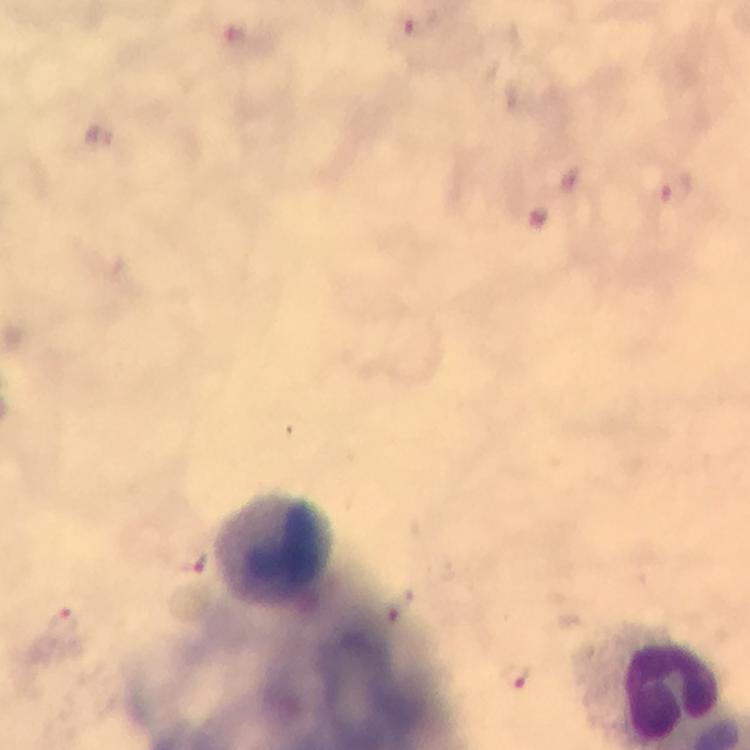

Approximate centers as (x, y) in pixels.
Summary:
  - Malaria parasite locations: (413, 25), (97, 136), (678, 189), (191, 562), (404, 605), (63, 628), (517, 677)
  - Leukocyte locations: (275, 547)
  - Capture: smartphone photograph through a microscope
  - Magnification: 100x
  - Stain: Giemsa
  - Context: from a diagnostic examination for malaria
  - Preparation: thick smear
  - Cropped from: one field of view
  - Immersion oil: applied
  - Image size: 750×750 pixels